Assess this cell for malaria.
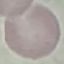
Uninfected.

Summary:
  - Image type: cell patch, automatically extracted from a larger field of view and resized to 64 × 64 pixels
  - Preparation: thin smear
  - Stain: Giemsa
  - Capture: smartphone through the microscope eyepiece